Give the extent of all uninfected red blood cells.
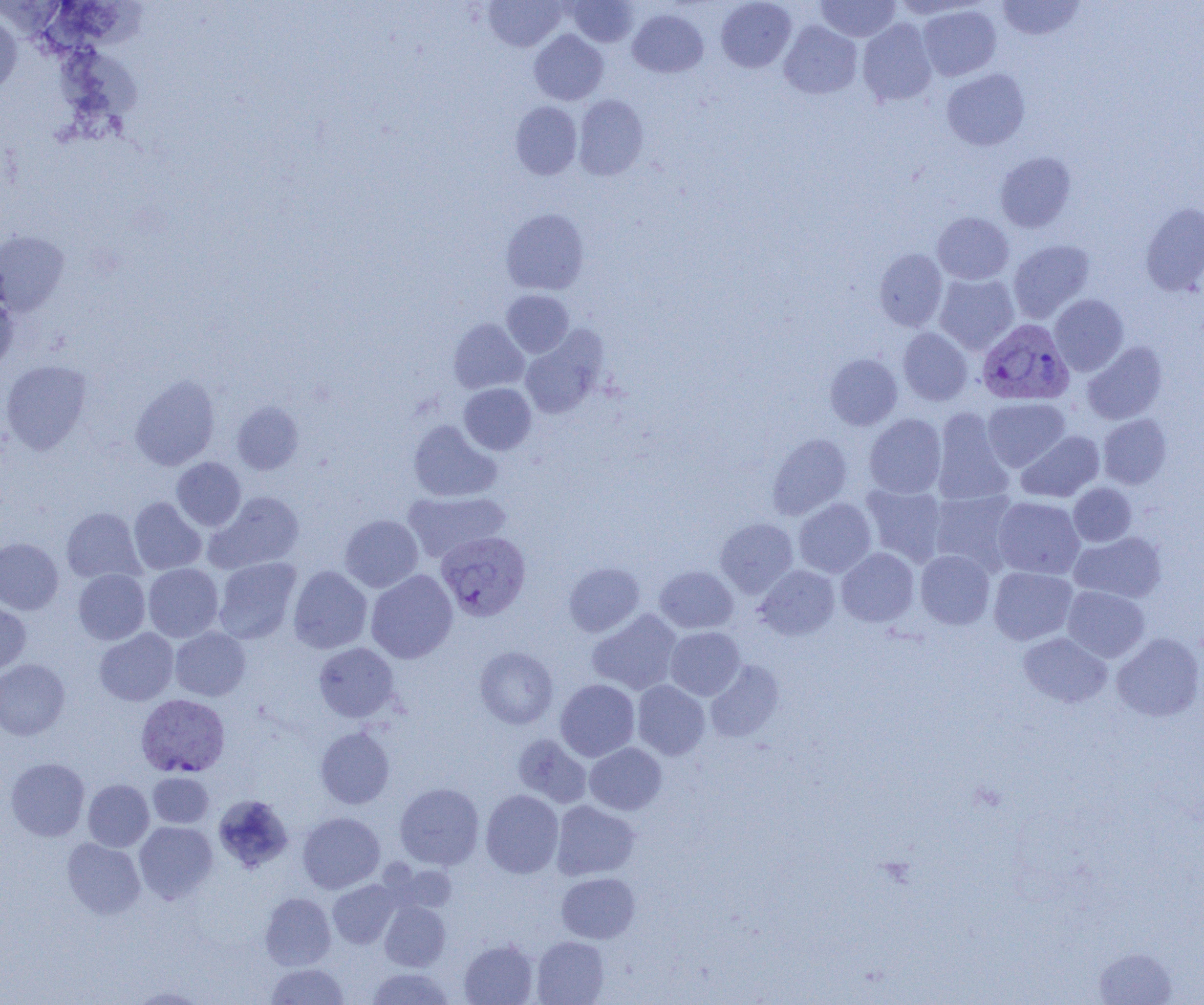
Approximate bounding boxes as (x1,y1)-(x2,y2) corner pairs in pixels.
Uninfected red blood cells: (484,0)-(566,51), (716,0)-(796,72), (816,0)-(899,42), (997,0)-(1086,41), (567,1)-(638,47), (32,3)-(153,61), (918,4)-(1001,81), (0,9)-(22,98), (628,9)-(708,77), (858,18)-(937,106), (779,21)-(862,99), (530,30)-(608,105), (55,51)-(147,121), (942,68)-(1030,150), (574,94)-(648,181), (510,101)-(582,179), (995,151)-(1076,232), (1141,202)-(1204,295), (501,208)-(589,295), (932,212)-(1014,284), (0,231)-(69,315), (1008,240)-(1095,323), (874,249)-(947,331), (934,273)-(1019,354), (501,290)-(574,357), (0,291)-(18,373), (1049,294)-(1129,376), (448,318)-(529,394), (520,327)-(607,419), (898,328)-(972,405), (1082,342)-(1167,424), (825,353)-(902,430), (1,359)-(92,454), (130,374)-(220,470), (459,383)-(536,455), (983,397)-(1070,471), (232,401)-(304,475), (931,409)-(1014,506), (864,414)-(947,498), (1098,414)-(1172,489), (408,420)-(501,502), (1016,430)-(1104,502), (767,433)-(852,520), (172,457)-(246,531), (860,483)-(948,566), (1068,483)-(1136,546), (929,489)-(1019,573), (403,490)-(510,562), (205,492)-(304,574), (128,497)-(206,575), (993,497)-(1085,579), (793,498)-(876,578), (62,508)-(144,584), (339,515)-(423,592), (715,518)-(798,597), (1070,532)-(1166,603), (0,537)-(63,614), (836,547)-(919,627), (915,550)-(995,629), (213,557)-(301,644), (143,563)-(223,641), (563,563)-(644,637), (754,564)-(840,640), (654,565)-(738,633), (288,566)-(372,653), (989,566)-(1078,645), (73,569)-(150,644), (366,570)-(458,663), (1062,585)-(1150,662), (0,599)-(30,675), (587,609)-(682,695), (665,626)-(745,700), (170,627)-(250,700), (94,628)-(178,706), (1019,632)-(1111,707), (1111,632)-(1204,722), (313,642)-(400,722), (475,646)-(558,728), (0,659)-(70,740), (705,660)-(784,742), (555,679)-(639,761), (632,681)-(710,760), (315,727)-(395,808), (512,733)-(591,807), (585,742)-(666,815), (6,757)-(90,841), (148,772)-(214,828), (83,779)-(154,851), (395,782)-(484,869), (481,790)-(563,878), (213,794)-(293,873), (551,800)-(640,880), (297,812)-(385,893), (134,821)-(218,903), (62,838)-(145,919), (390,862)-(457,915), (557,872)-(640,943), (327,879)-(402,948), (260,892)-(336,970), (380,901)-(450,971), (531,936)-(609,1005), (459,939)-(538,1005), (1092,946)-(1179,1005), (266,963)-(349,1005), (365,967)-(456,1004), (127,987)-(209,1004).

Summary:
  - Plasmodium vivax-infected red blood cell locations: (977,319)-(1074,406), (436,534)-(532,624), (135,693)-(230,777)
  - Slide-level diagnosis: Plasmodium vivax
  - Image size: 1204×1005 pixels
  - Field of view: single
  - Modality: light microscopy
  - Magnification: 1000x
  - Preparation: thin blood film